Classify this cell by malaria status.
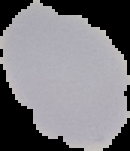
It is uninfected.

Summary:
  - Preparation: thin blood smear
  - Image type: cell region segmented out of the field of view; surrounding area masked to black
  - Image size: 130×151 pixels